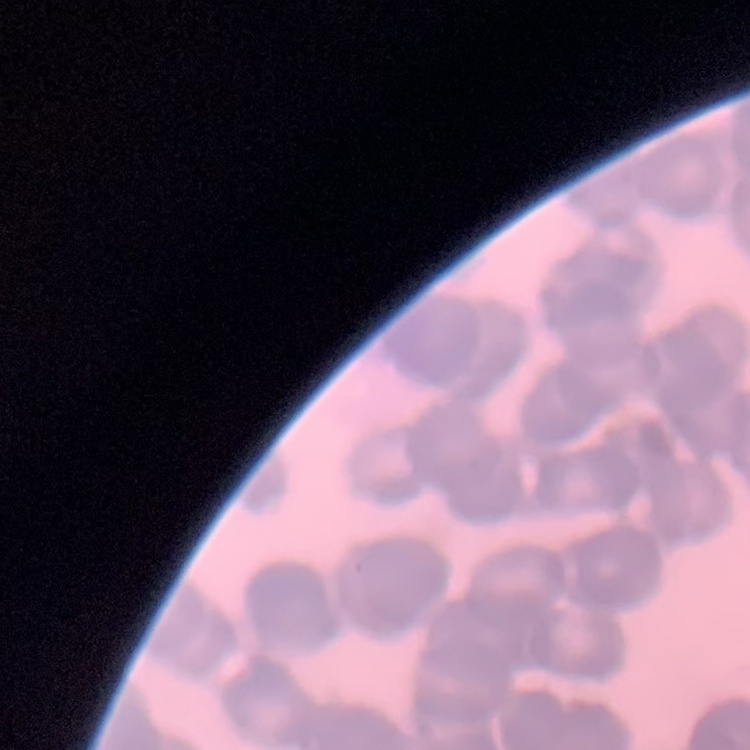 The erythrocytes exhibit rouleaux formation. One tile cut from a larger photomicrograph. Thin peripheral smear. Field's or Giemsa stain.